Name the parasite shown.
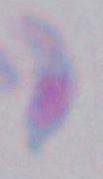

This is Toxoplasma gondii.

modality = photomicrograph
magnification = 1000x